Classify this cell by malaria status.
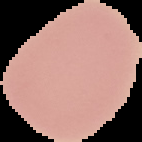
It is uninfected.

Segmented cell region on a black background. Image is 142×142 pixels. From a thin blood smear.